Evaluate for Plasmodium parasites.
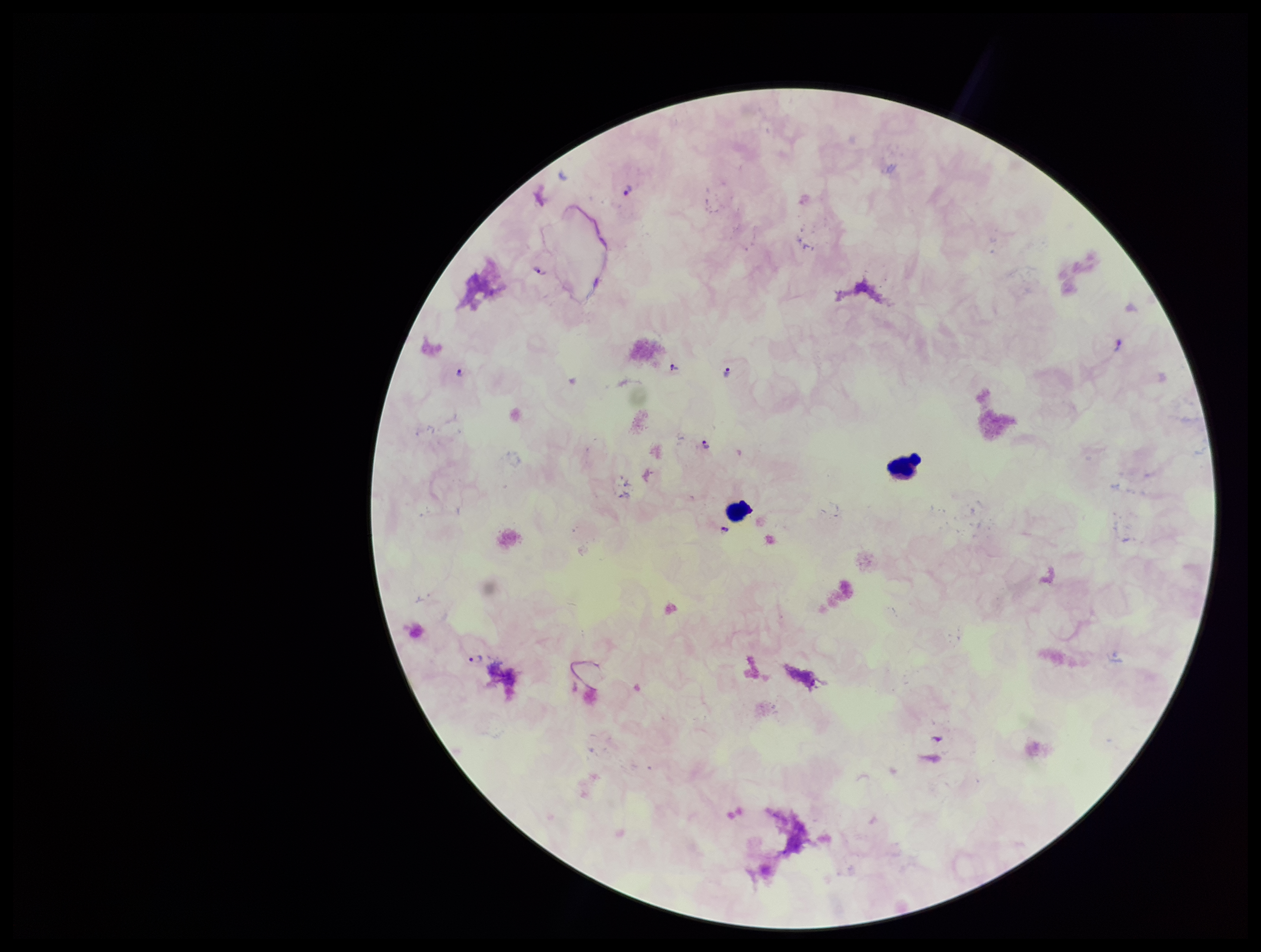
Detected.

Summary:
  - Preparation: thick
  - Stain: Giemsa
  - Leukocyte count: 2
  - Field of view: single
  - Species reported for this patient: Plasmodium falciparum
  - Image size: 1261×952 pixels
  - Patient malaria status: infected
  - Parasite count: 7
  - Capture: smartphone photograph through the microscope eyepiece